Outline each white blood cell.
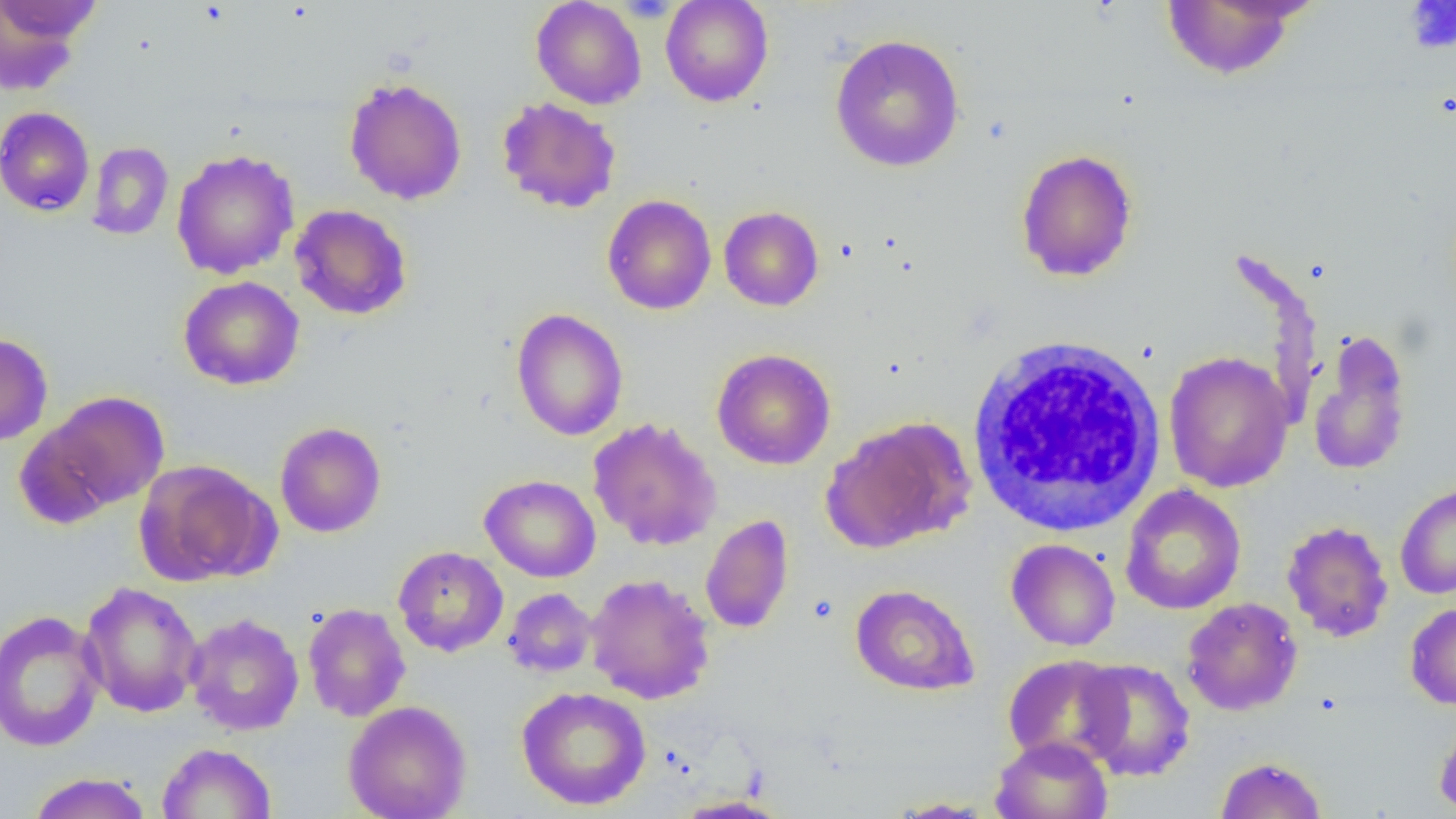

Approximate bounding boxes as named x1/y1/x2/y2 corners in pixels.
White blood cells: (x1=966, y1=333, x2=1168, y2=537).

Platelet locations: (x1=1404, y1=1, x2=1456, y2=54). Uninfected red blood cell locations: (x1=531, y1=0, x2=646, y2=109), (x1=661, y1=0, x2=774, y2=107), (x1=1, y1=1, x2=104, y2=47), (x1=1160, y1=1, x2=1308, y2=81), (x1=0, y1=2, x2=99, y2=97), (x1=829, y1=33, x2=966, y2=172), (x1=343, y1=77, x2=468, y2=205), (x1=496, y1=97, x2=621, y2=214), (x1=0, y1=106, x2=95, y2=217), (x1=87, y1=142, x2=174, y2=241), (x1=172, y1=149, x2=299, y2=279), (x1=1015, y1=149, x2=1139, y2=282), (x1=602, y1=194, x2=717, y2=315), (x1=290, y1=204, x2=412, y2=321), (x1=719, y1=206, x2=824, y2=311), (x1=178, y1=276, x2=305, y2=391), (x1=511, y1=308, x2=628, y2=441), (x1=1307, y1=329, x2=1413, y2=478), (x1=0, y1=332, x2=53, y2=445), (x1=712, y1=349, x2=835, y2=470), (x1=1163, y1=351, x2=1294, y2=493), (x1=33, y1=390, x2=172, y2=517), (x1=822, y1=416, x2=975, y2=553), (x1=587, y1=417, x2=722, y2=552), (x1=274, y1=421, x2=386, y2=538), (x1=135, y1=459, x2=279, y2=586), (x1=480, y1=474, x2=601, y2=582), (x1=1395, y1=482, x2=1456, y2=599), (x1=1120, y1=485, x2=1246, y2=615), (x1=700, y1=514, x2=794, y2=634), (x1=1281, y1=521, x2=1394, y2=642), (x1=1006, y1=539, x2=1120, y2=651), (x1=393, y1=545, x2=508, y2=657), (x1=586, y1=573, x2=715, y2=705), (x1=79, y1=581, x2=204, y2=718), (x1=850, y1=583, x2=979, y2=696), (x1=503, y1=587, x2=597, y2=678), (x1=1181, y1=597, x2=1303, y2=715), (x1=302, y1=602, x2=411, y2=722), (x1=1405, y1=602, x2=1456, y2=710), (x1=0, y1=608, x2=106, y2=752), (x1=184, y1=613, x2=304, y2=736), (x1=1002, y1=654, x2=1128, y2=768), (x1=1075, y1=658, x2=1196, y2=781), (x1=516, y1=686, x2=651, y2=811), (x1=343, y1=700, x2=473, y2=819), (x1=1434, y1=713, x2=1456, y2=816), (x1=990, y1=736, x2=1112, y2=819), (x1=156, y1=742, x2=277, y2=818), (x1=1215, y1=756, x2=1327, y2=819), (x1=26, y1=772, x2=153, y2=819), (x1=670, y1=794, x2=792, y2=818), (x1=883, y1=796, x2=998, y2=817). Slide-level diagnosis: negative for blood parasites. Light microscopy. One field of a larger specimen. Captured at 1000x magnification. Image is 1456×819 pixels. Thin blood smear.